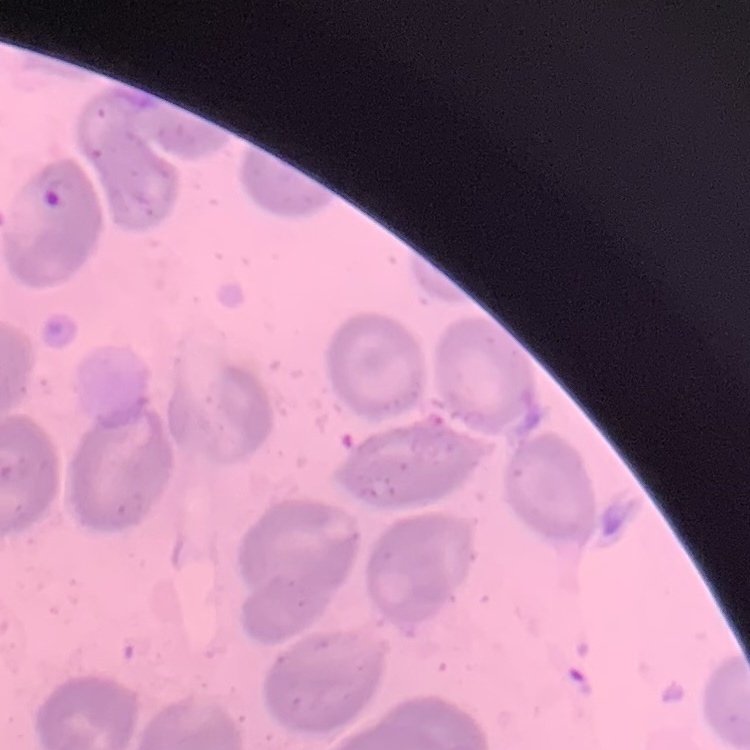 The red blood cells show no rouleaux formation. One tile cut from a larger photomicrograph. Stained with either Field's or Giemsa. Thin blood smear.